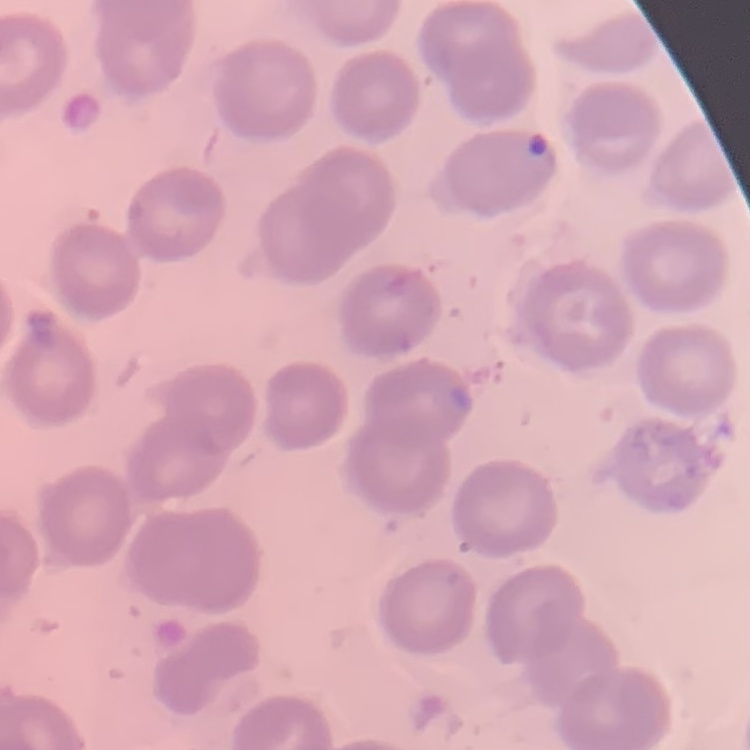
Summary:
  - Erythrocyte morphology: no rouleaux formation
  - Preparation: thin blood film
  - Image type: square crop of a larger photomicrograph
  - Stain: Field's or Giemsa